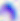 400x magnification. Photomicrograph. Toxoplasma gondii is seen.